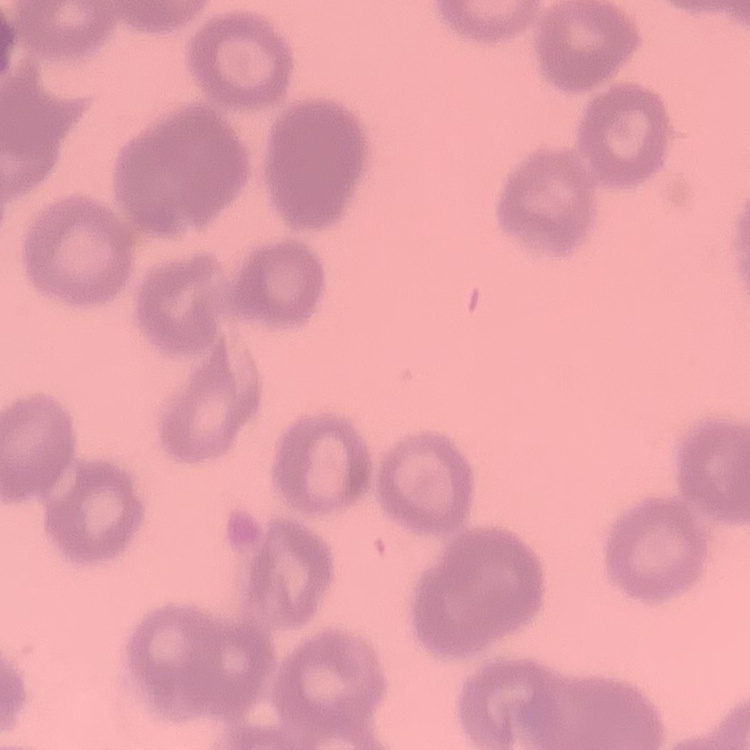
The red blood cells exhibit rouleaux formation. Field's or Giemsa stain. One tile cut from a larger photomicrograph. Thin blood smear.